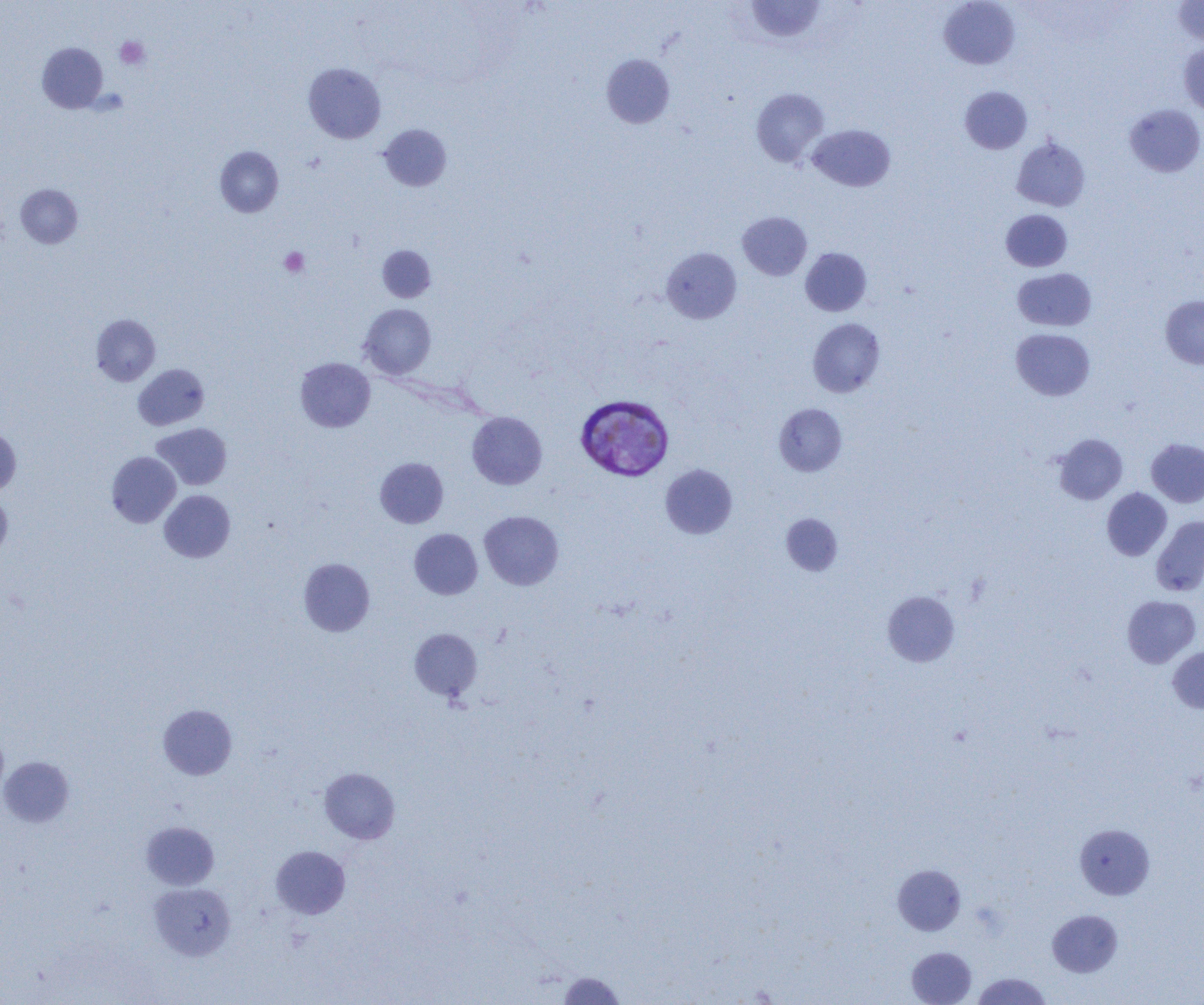

Summary:
  - Coordinate format: approximate bounding boxes as named x1/y1/x2/y2 corners in pixels
  - Plasmodium vivax-infected red blood cell locations: (x1=576, y1=394, x2=674, y2=480)
  - Platelet locations: (x1=114, y1=36, x2=150, y2=69), (x1=279, y1=247, x2=309, y2=277)
  - Uninfected red blood cell locations: (x1=746, y1=0, x2=825, y2=42), (x1=939, y1=1, x2=1020, y2=69), (x1=1173, y1=1, x2=1204, y2=47), (x1=37, y1=42, x2=108, y2=113), (x1=1179, y1=43, x2=1204, y2=116), (x1=601, y1=54, x2=675, y2=128), (x1=303, y1=62, x2=386, y2=143), (x1=959, y1=86, x2=1032, y2=154), (x1=751, y1=88, x2=829, y2=167), (x1=1125, y1=104, x2=1204, y2=177), (x1=379, y1=124, x2=452, y2=191), (x1=807, y1=124, x2=895, y2=191), (x1=1011, y1=138, x2=1090, y2=211), (x1=215, y1=146, x2=283, y2=217), (x1=15, y1=184, x2=83, y2=248), (x1=1001, y1=209, x2=1072, y2=271), (x1=737, y1=212, x2=811, y2=280), (x1=377, y1=245, x2=436, y2=302), (x1=661, y1=247, x2=741, y2=323), (x1=800, y1=247, x2=872, y2=316), (x1=1013, y1=268, x2=1096, y2=331), (x1=1161, y1=295, x2=1204, y2=368), (x1=359, y1=303, x2=436, y2=379), (x1=91, y1=314, x2=161, y2=385), (x1=807, y1=318, x2=885, y2=397), (x1=1011, y1=328, x2=1095, y2=401), (x1=295, y1=357, x2=375, y2=432), (x1=133, y1=364, x2=209, y2=430), (x1=774, y1=403, x2=847, y2=476), (x1=467, y1=411, x2=547, y2=489), (x1=151, y1=423, x2=231, y2=490), (x1=0, y1=427, x2=21, y2=494), (x1=1053, y1=434, x2=1127, y2=505), (x1=1146, y1=438, x2=1204, y2=507), (x1=107, y1=451, x2=181, y2=527), (x1=375, y1=457, x2=449, y2=528), (x1=660, y1=464, x2=737, y2=539), (x1=1102, y1=487, x2=1171, y2=561), (x1=159, y1=490, x2=236, y2=562), (x1=0, y1=491, x2=12, y2=556), (x1=479, y1=510, x2=564, y2=590), (x1=781, y1=513, x2=842, y2=576), (x1=1151, y1=516, x2=1204, y2=596), (x1=409, y1=529, x2=483, y2=599), (x1=298, y1=558, x2=375, y2=636), (x1=882, y1=591, x2=960, y2=666), (x1=1122, y1=595, x2=1201, y2=668), (x1=409, y1=628, x2=482, y2=701), (x1=1167, y1=646, x2=1204, y2=713), (x1=158, y1=704, x2=237, y2=780), (x1=0, y1=727, x2=8, y2=801), (x1=0, y1=756, x2=74, y2=827), (x1=319, y1=767, x2=400, y2=844), (x1=141, y1=821, x2=219, y2=890), (x1=1074, y1=823, x2=1155, y2=899), (x1=270, y1=846, x2=350, y2=919), (x1=892, y1=864, x2=966, y2=935), (x1=149, y1=882, x2=235, y2=961), (x1=1047, y1=910, x2=1123, y2=977), (x1=906, y1=947, x2=976, y2=1005), (x1=558, y1=972, x2=626, y2=1004), (x1=972, y1=972, x2=1052, y2=1004)
  - Slide-level diagnosis: Plasmodium vivax
  - Magnification: 1000x
  - Preparation: thin blood smear
  - Field of view: one of a larger specimen
  - Modality: light microscopy
  - Image size: 1204×1005 pixels